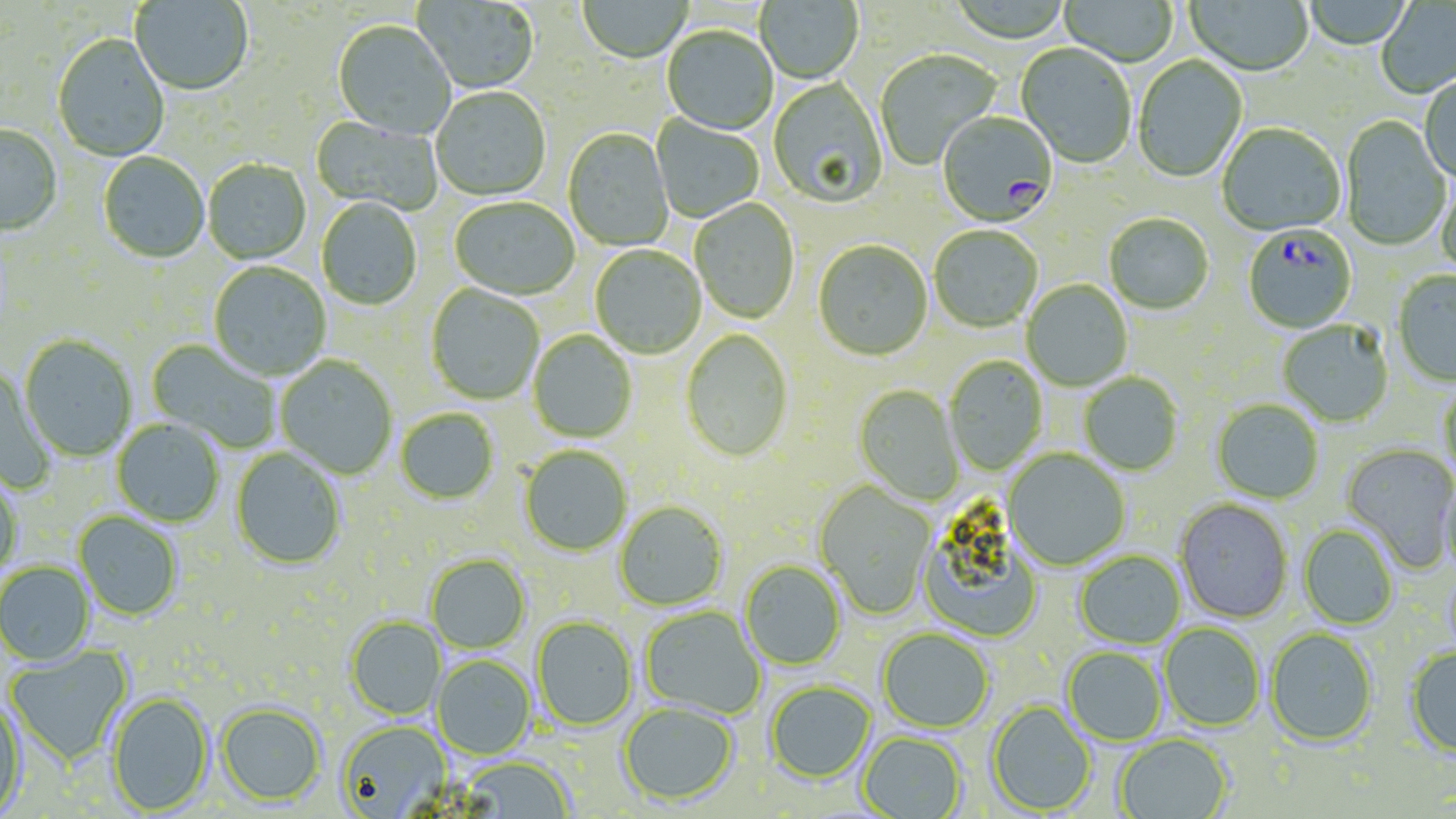
slide-level diagnosis = Plasmodium falciparum
uninfected red blood cell locations = approximate bounding boxes as (x1, y1, x2, y2) in pixels: (414, 0, 540, 96), (1059, 0, 1178, 68), (1186, 0, 1313, 79), (1301, 0, 1414, 52), (130, 1, 253, 97), (578, 1, 692, 65), (756, 1, 863, 86), (1376, 2, 1456, 99), (332, 22, 456, 141), (662, 27, 778, 136), (52, 34, 170, 163), (1016, 44, 1136, 170), (875, 49, 1002, 171), (1133, 56, 1248, 184), (1419, 76, 1456, 184), (768, 79, 889, 210), (431, 88, 551, 202), (651, 114, 765, 223), (310, 116, 443, 216), (1340, 116, 1451, 252), (1217, 124, 1345, 237), (0, 126, 63, 239), (563, 129, 673, 251), (97, 152, 209, 264), (203, 160, 311, 265), (1435, 170, 1456, 280), (449, 198, 579, 302), (316, 199, 423, 311), (689, 199, 799, 325), (1104, 215, 1213, 316), (929, 226, 1043, 333), (813, 241, 933, 363), (590, 246, 706, 360), (208, 262, 330, 381), (1393, 272, 1456, 387), (1022, 280, 1133, 391), (426, 285, 544, 406), (1278, 321, 1393, 427), (528, 330, 638, 443), (680, 330, 793, 463), (19, 335, 137, 462), (146, 339, 282, 452), (944, 355, 1048, 475), (276, 356, 398, 479), (0, 367, 57, 493), (1079, 372, 1183, 476), (1438, 380, 1456, 481), (854, 384, 964, 506), (1212, 400, 1323, 504), (395, 409, 499, 505), (111, 419, 225, 527), (1341, 444, 1456, 573), (520, 446, 632, 557), (231, 447, 346, 570), (1004, 449, 1130, 571), (0, 471, 23, 577), (1439, 473, 1456, 579), (813, 481, 936, 620), (1175, 500, 1293, 623), (615, 501, 729, 611), (74, 511, 183, 621), (919, 518, 1043, 644), (1298, 525, 1399, 630), (1074, 551, 1186, 649), (426, 554, 531, 654), (740, 561, 846, 671), (0, 562, 94, 665), (1442, 563, 1456, 662), (641, 606, 766, 720), (346, 616, 445, 719), (531, 617, 637, 732), (1160, 624, 1265, 732), (877, 628, 994, 733), (1265, 628, 1378, 747), (5, 646, 133, 765), (1062, 647, 1167, 746), (1405, 647, 1456, 758), (432, 655, 535, 759), (765, 682, 876, 784), (107, 692, 213, 815), (0, 693, 27, 817), (986, 701, 1097, 815), (217, 702, 326, 806), (618, 702, 738, 807), (336, 720, 451, 818), (858, 732, 966, 819), (1114, 734, 1233, 819), (458, 756, 574, 818)
image size = 1456×819 pixels
magnification = 1000x
modality = light microscopy
Plasmodium falciparum-infected red blood cell locations = approximate bounding boxes as (x1, y1, x2, y2) in pixels: (937, 113, 1058, 228), (1244, 226, 1357, 334)
field of view = single
preparation = thin blood film
stain = May-Grünwald-Giemsa